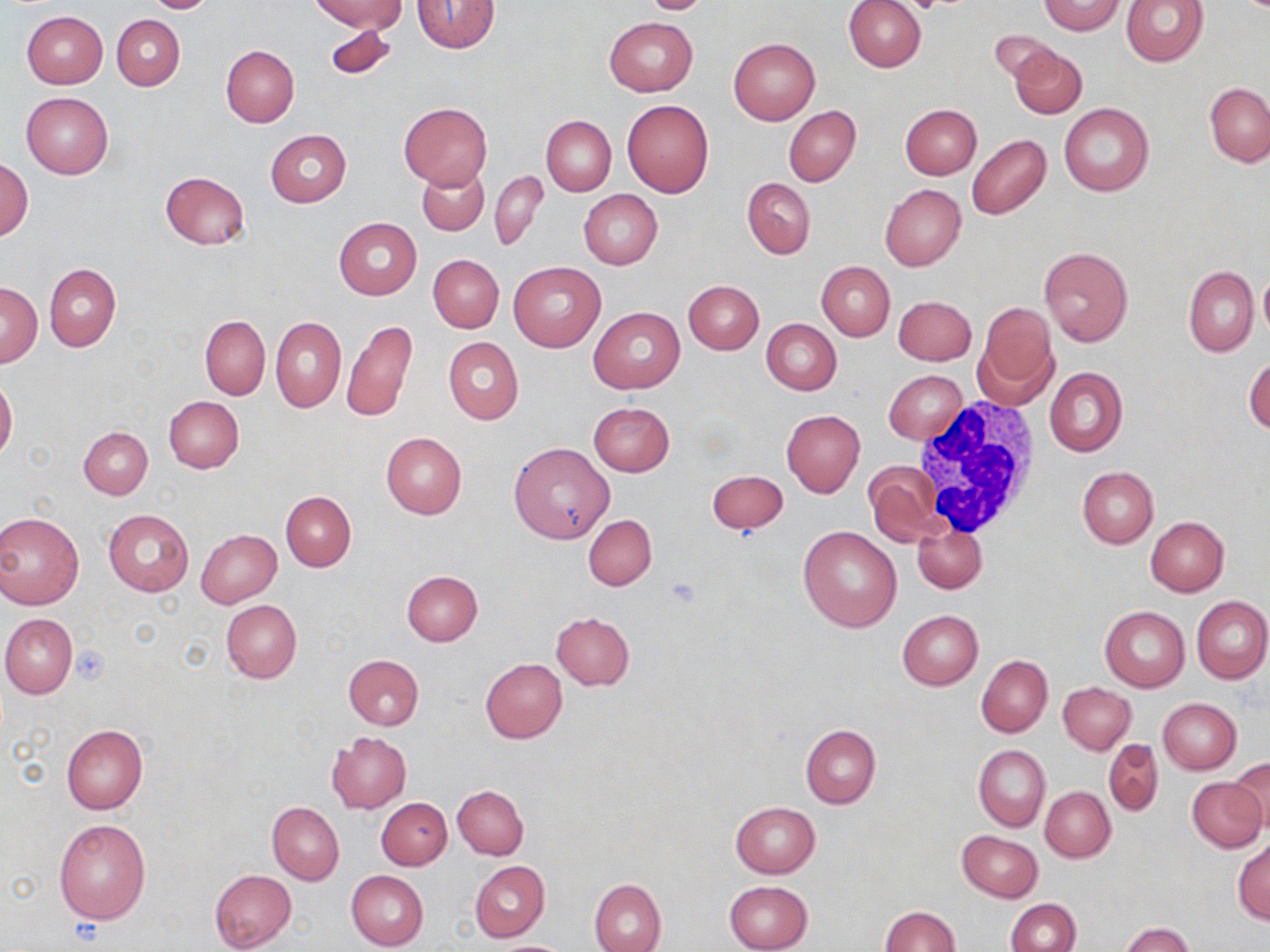

slide-level diagnosis = no evidence of blood parasites
image size = 1270×952 pixels
white blood cell locations = approximate bounding boxes as (x1, y1, x2, y2) in pixels: (907, 396, 1046, 542)
preparation = thin blood smear
field of view = single
stain = May-Grünwald-Giemsa
platelet locations = approximate bounding boxes as (x1, y1, x2, y2) in pixels: (904, 0, 948, 13), (666, 576, 702, 606), (70, 645, 109, 683)
modality = light microscopy
uninfected red blood cell locations = approximate bounding boxes as (x1, y1, x2, y2) in pixels: (146, 0, 214, 13), (311, 0, 407, 33), (639, 0, 713, 14), (843, 0, 925, 72), (1120, 0, 1209, 67), (412, 1, 500, 53), (1038, 1, 1125, 35), (21, 11, 108, 88), (113, 15, 185, 90), (603, 17, 697, 96), (326, 25, 396, 80), (990, 30, 1060, 86), (728, 38, 819, 125), (221, 44, 299, 126), (1009, 45, 1086, 119), (1205, 82, 1270, 167), (21, 92, 112, 178), (623, 100, 715, 197), (398, 103, 492, 190), (1059, 103, 1154, 195), (901, 104, 982, 179), (783, 106, 860, 186), (542, 115, 615, 195), (265, 129, 351, 207), (966, 135, 1051, 219), (1, 158, 33, 240), (418, 164, 488, 235), (160, 170, 251, 250), (490, 170, 547, 250), (742, 178, 815, 259), (880, 183, 965, 271), (579, 189, 662, 269), (334, 218, 421, 300), (1039, 245, 1132, 347), (428, 254, 504, 333), (816, 261, 894, 340), (508, 262, 605, 352), (45, 264, 121, 350), (1184, 265, 1259, 357), (1257, 267, 1270, 341), (683, 280, 764, 354), (1, 284, 41, 367), (893, 295, 976, 366), (973, 301, 1058, 407), (591, 307, 684, 393), (200, 316, 270, 399), (271, 316, 346, 412), (761, 318, 842, 395), (343, 320, 418, 425), (444, 337, 523, 425), (1244, 354, 1270, 435), (1044, 366, 1127, 456), (883, 369, 967, 444), (0, 377, 17, 459), (163, 396, 243, 473), (588, 402, 674, 476), (781, 410, 864, 497), (79, 427, 153, 499), (381, 432, 467, 518), (509, 442, 615, 545), (863, 461, 944, 548), (1077, 466, 1158, 548), (706, 470, 788, 534), (281, 492, 355, 570), (103, 508, 194, 596), (0, 510, 85, 609), (583, 514, 657, 590), (1146, 517, 1229, 597), (912, 522, 986, 594), (798, 525, 903, 632), (197, 530, 282, 608), (402, 571, 483, 646), (1192, 595, 1270, 684), (220, 598, 302, 683), (1100, 606, 1189, 691), (897, 610, 984, 690), (550, 612, 634, 691), (1, 613, 76, 698), (344, 654, 425, 730), (976, 654, 1052, 738), (481, 657, 568, 743), (1058, 682, 1136, 754), (1157, 697, 1241, 774), (61, 724, 149, 813), (800, 724, 880, 809), (327, 732, 411, 813), (1104, 739, 1163, 817), (973, 745, 1049, 830), (1229, 756, 1270, 837), (1188, 777, 1266, 852), (453, 784, 528, 858), (1040, 786, 1115, 861), (377, 798, 452, 870), (730, 801, 821, 878), (268, 803, 344, 885), (53, 818, 151, 923), (958, 831, 1043, 902), (1233, 838, 1270, 924), (470, 861, 550, 941), (209, 869, 296, 951), (346, 869, 429, 950), (589, 878, 667, 952), (724, 880, 813, 952), (1006, 899, 1080, 952), (879, 906, 959, 952), (1120, 921, 1194, 952)
magnification = 1000x